Report the malaria status of this cell.
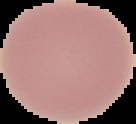
Uninfected.

Summary:
  - Preparation: thin blood smear
  - Image size: 136×124 pixels
  - Image type: cell region segmented out of the field of view; surrounding area masked to black